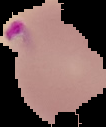
preparation = thin blood film
malaria status = parasitized
image size = 106×127 pixels
image type = segmented cell region with the area outside set to black